Assess the morphology of the erythrocytes.
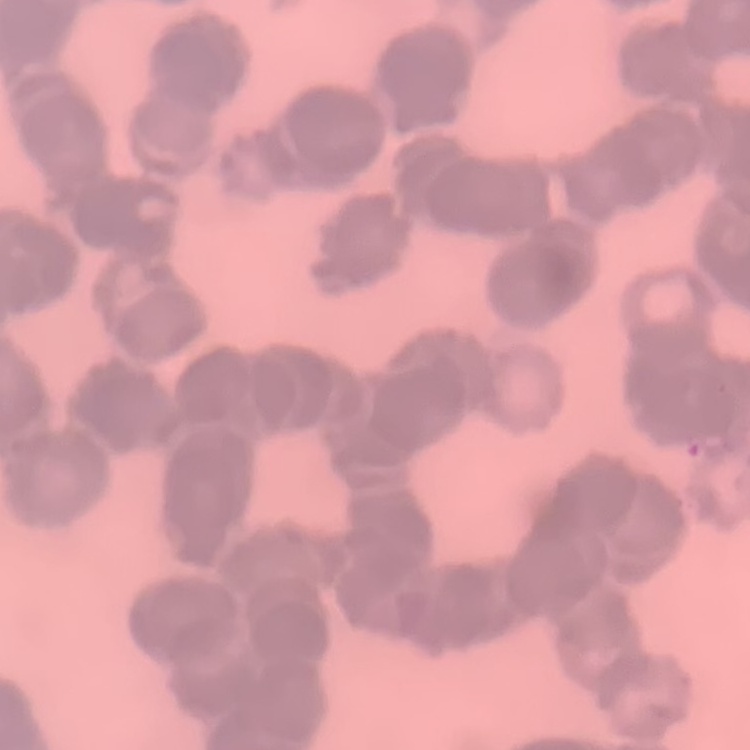
Rouleaux formation.

{
  "image_type": "one tile cut from a larger photomicrograph",
  "preparation": "thin peripheral smear",
  "stain": "Field's or Giemsa"
}